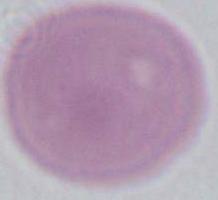

A red blood cell is seen. 1000x magnification. Micrograph.